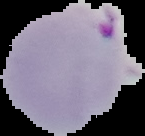
{
  "preparation": "thin blood film",
  "image_size": "145×136 pixels",
  "image_type": "segmented cell region with the area outside set to black",
  "malaria_status": "parasitized"
}